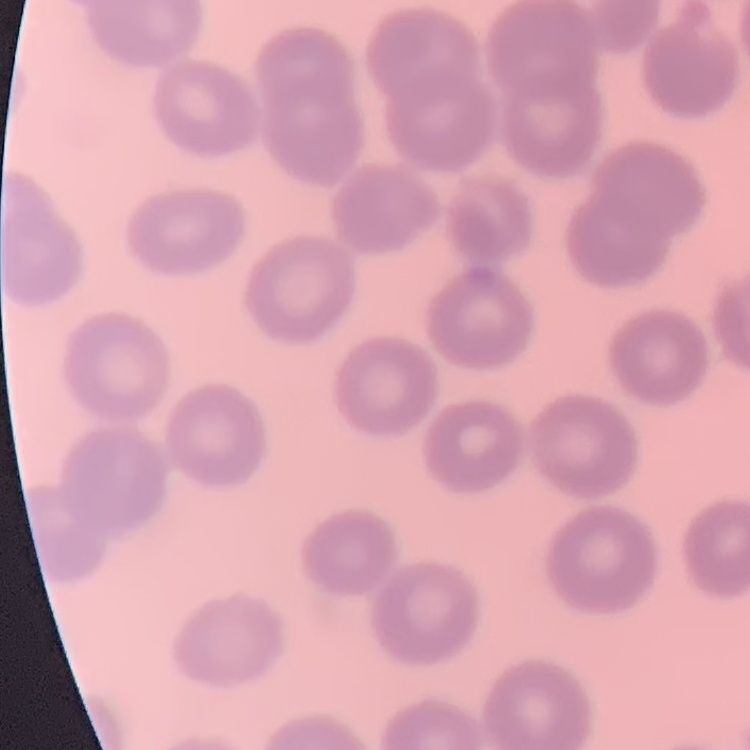

Summary:
  - Red blood cell morphology: no rouleaux formation
  - Stain: Field's or Giemsa
  - Image type: one tile cut from a larger photomicrograph
  - Preparation: thin blood film